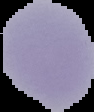

Summary:
  - Preparation: thin blood film
  - Image size: 94×112 pixels
  - Image type: cell region segmented out of the field of view; surrounding area masked to black
  - Malaria status: uninfected